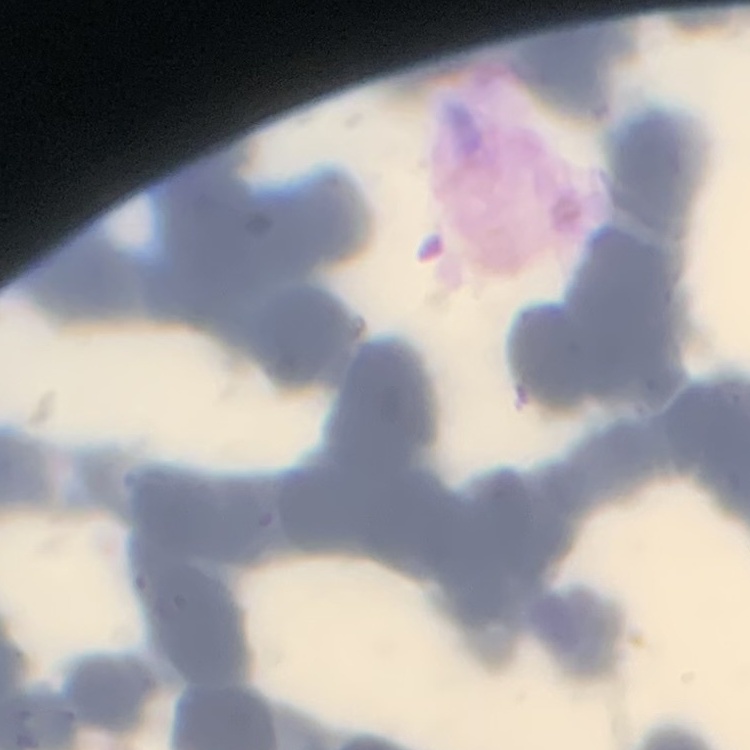
Summary:
  - Red blood cell morphology: rouleaux formation
  - Preparation: thin peripheral smear
  - Stain: Field's or Giemsa
  - Image type: one tile cut from a larger photomicrograph